Identify the cell.
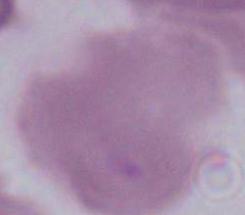
This is an erythrocyte.

Photomicrograph. Captured at 1000x magnification.